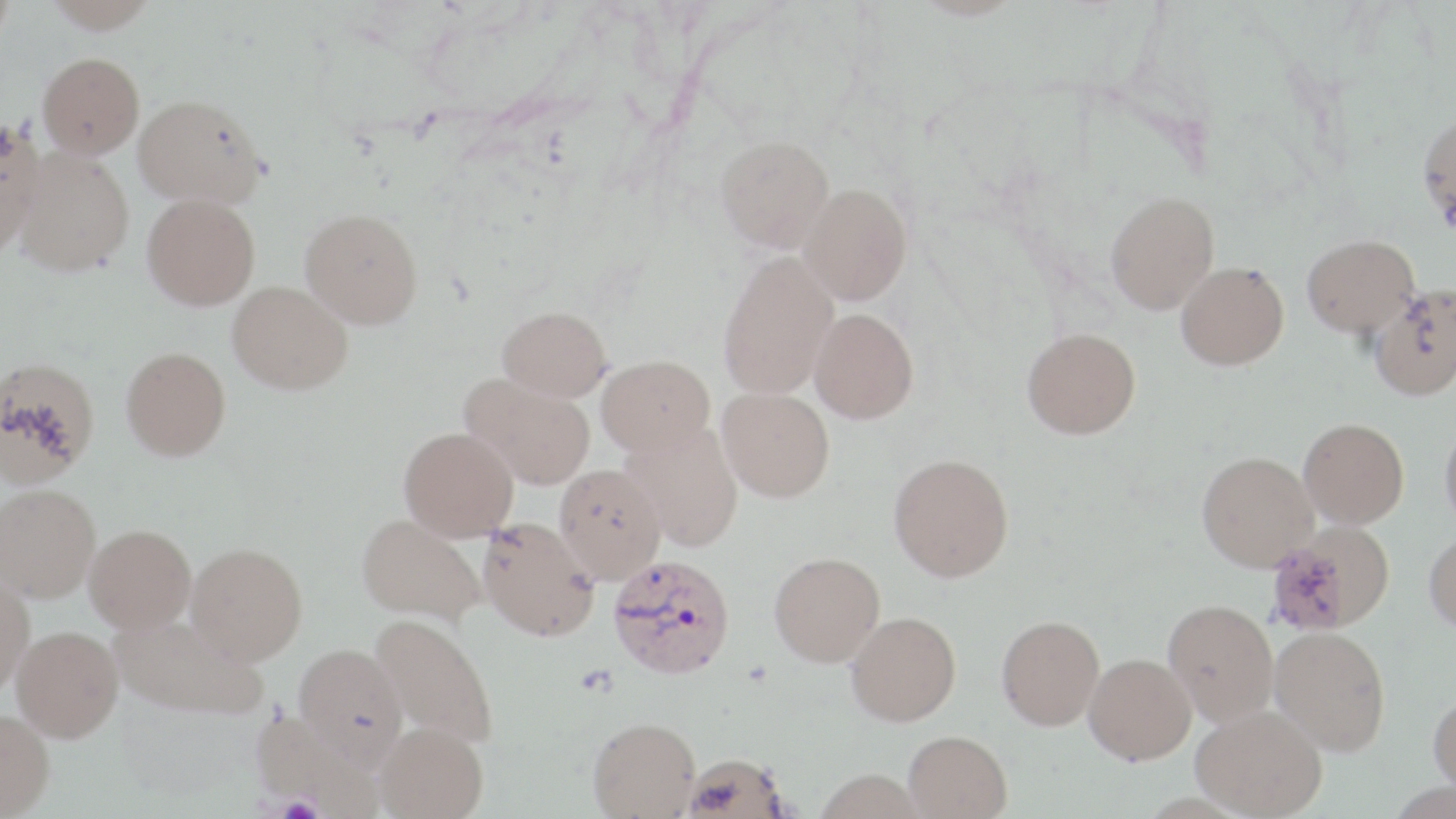

Summary:
  - Coordinate format: approximate bounding boxes as named x1/y1/x2/y2 corners in pixels
  - Uninfected red blood cell locations: (x1=0, y1=0, x2=15, y2=52), (x1=44, y1=0, x2=158, y2=33), (x1=38, y1=52, x2=144, y2=157), (x1=134, y1=94, x2=266, y2=208), (x1=1418, y1=111, x2=1456, y2=231), (x1=0, y1=122, x2=45, y2=256), (x1=716, y1=135, x2=835, y2=252), (x1=13, y1=147, x2=135, y2=276), (x1=800, y1=183, x2=912, y2=304), (x1=1105, y1=191, x2=1220, y2=314), (x1=142, y1=193, x2=260, y2=310), (x1=300, y1=208, x2=423, y2=329), (x1=1302, y1=234, x2=1419, y2=337), (x1=717, y1=250, x2=839, y2=400), (x1=1176, y1=261, x2=1289, y2=370), (x1=228, y1=280, x2=352, y2=394), (x1=1369, y1=287, x2=1456, y2=401), (x1=497, y1=305, x2=612, y2=401), (x1=810, y1=307, x2=919, y2=423), (x1=1022, y1=327, x2=1141, y2=439), (x1=121, y1=346, x2=231, y2=460), (x1=596, y1=354, x2=714, y2=456), (x1=0, y1=355, x2=100, y2=488), (x1=460, y1=374, x2=595, y2=489), (x1=717, y1=387, x2=835, y2=502), (x1=1298, y1=417, x2=1409, y2=528), (x1=1440, y1=417, x2=1456, y2=533), (x1=622, y1=422, x2=744, y2=551), (x1=399, y1=426, x2=518, y2=540), (x1=1197, y1=451, x2=1319, y2=571), (x1=889, y1=453, x2=1014, y2=581), (x1=554, y1=464, x2=666, y2=583), (x1=0, y1=483, x2=100, y2=602), (x1=357, y1=514, x2=485, y2=624), (x1=477, y1=517, x2=600, y2=641), (x1=1268, y1=522, x2=1396, y2=636), (x1=85, y1=524, x2=196, y2=631), (x1=1424, y1=530, x2=1456, y2=634), (x1=186, y1=543, x2=308, y2=664), (x1=769, y1=551, x2=885, y2=666), (x1=0, y1=570, x2=35, y2=694), (x1=1163, y1=599, x2=1279, y2=726), (x1=846, y1=611, x2=961, y2=726), (x1=110, y1=612, x2=265, y2=720), (x1=371, y1=613, x2=499, y2=748), (x1=997, y1=615, x2=1105, y2=730), (x1=12, y1=626, x2=124, y2=741), (x1=1270, y1=626, x2=1391, y2=755), (x1=294, y1=644, x2=408, y2=764), (x1=1084, y1=653, x2=1196, y2=763), (x1=1428, y1=691, x2=1456, y2=794), (x1=1191, y1=704, x2=1327, y2=818), (x1=0, y1=710, x2=54, y2=818), (x1=588, y1=717, x2=701, y2=817), (x1=376, y1=722, x2=489, y2=819), (x1=903, y1=730, x2=1013, y2=819), (x1=680, y1=753, x2=790, y2=818)
  - Platelet locations: (x1=274, y1=797, x2=326, y2=819)
  - Plasmodium vivax-infected red blood cell locations: (x1=607, y1=554, x2=735, y2=678)
  - Slide-level diagnosis: Plasmodium vivax
  - Modality: optical microscopy
  - Preparation: thin blood smear
  - Field of view: single
  - Magnification: 1000x
  - Stain: May-Grünwald-Giemsa
  - Image size: 1456×819 pixels